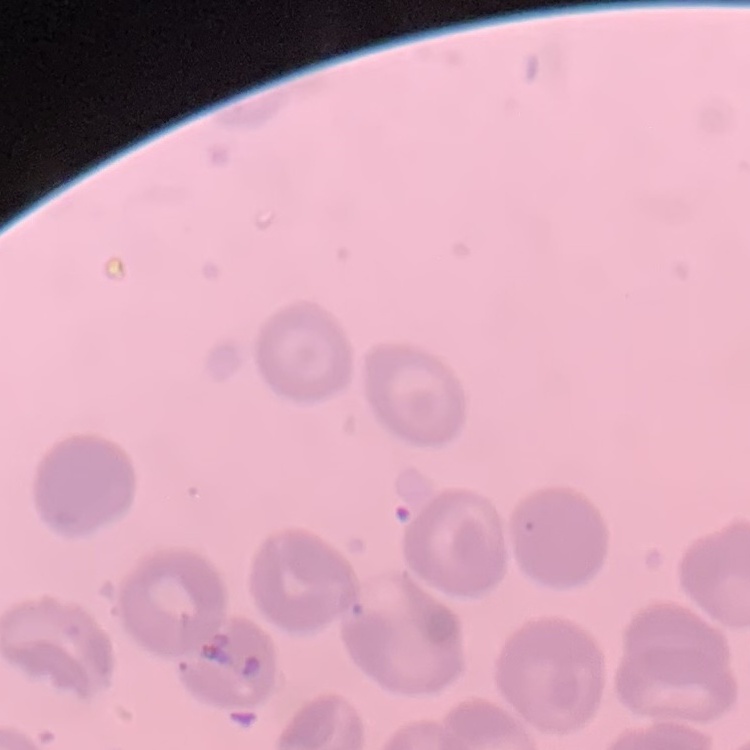

Summary:
  - Erythrocyte morphology: no rouleaux formation
  - Stain: Field's or Giemsa
  - Preparation: thin peripheral smear
  - Image type: one tile cut from a larger photomicrograph